Point out each Plasmodium parasite.
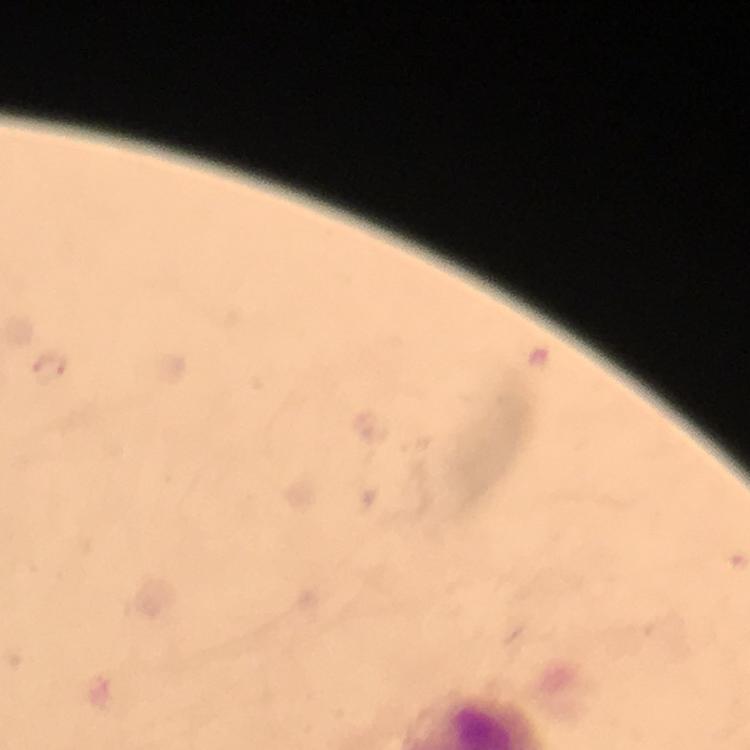
Approximate centers as (x, y) in pixels.
Plasmodium parasites: (51, 368).

immersion_oil: applied
preparation: thick blood smear
stain: Giemsa
capture: smartphone photograph through a microscope
image_size: 750×750 pixels
context: from a diagnostic examination for malaria
magnification: 100x
cropped_from: a single field of view